Outline each blood parasite and name the species.
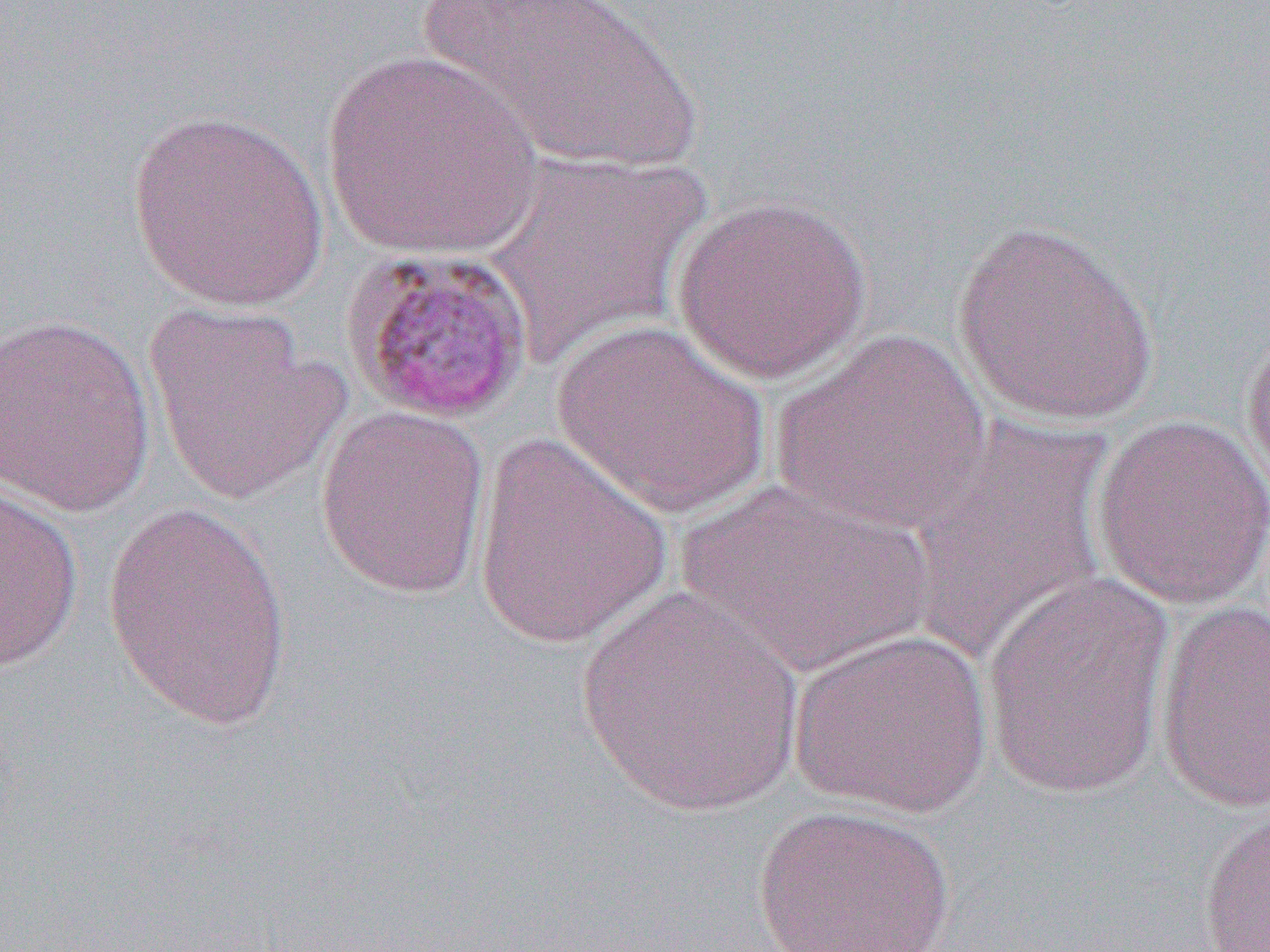
Approximate bounding boxes as [x1, y1, x2, y2] in pixels.
Plasmodium malariae-infected red blood cells: [337, 242, 536, 425].
No Plasmodium falciparum, Plasmodium ovale, Plasmodium vivax, Babesia divergens, or Trypanosoma brucei observed.

Summary:
  - Uninfected red blood cell locations: [413, 0, 710, 177], [320, 49, 544, 258], [125, 108, 332, 311], [481, 150, 711, 369], [670, 194, 872, 384], [951, 219, 1161, 427], [143, 303, 350, 506], [0, 312, 157, 516], [1240, 317, 1270, 506], [551, 318, 770, 518], [771, 328, 990, 535], [314, 404, 491, 599], [906, 415, 1116, 663], [1090, 415, 1270, 611], [472, 431, 674, 652], [676, 476, 934, 677], [0, 481, 84, 674], [101, 502, 297, 731], [980, 570, 1176, 798], [576, 586, 806, 823], [1154, 600, 1270, 815], [790, 627, 994, 819], [1196, 799, 1270, 951], [750, 803, 955, 952]
  - Slide-level diagnosis: Plasmodium malariae
  - Field of view: one of a larger specimen
  - Image size: 1270×952 pixels
  - Modality: light microscopy
  - Preparation: thin blood smear
  - Magnification: 1000x